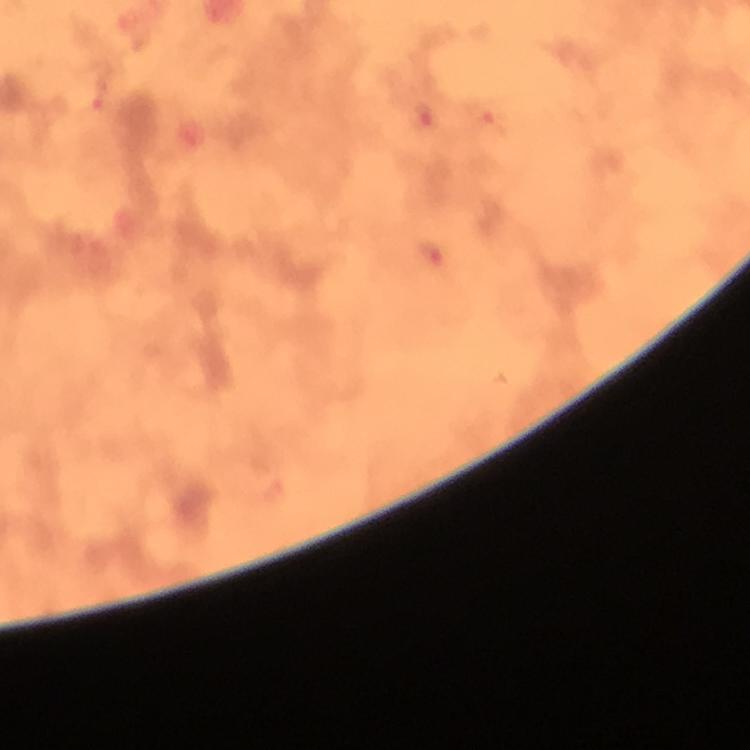
cropped_from: a single field of view
stain: Giemsa
preparation: thick smear
image_size: 750×750 pixels
immersion_oil: applied
magnification: 100x
malaria_parasite_locations: 'approximate centers as (x, y) in pixels: (98, 92), (420, 117), (487, 119), (431, 255)'
context: from a malaria diagnostic workup
capture: smartphone photograph through a microscope